Point out every Plasmodium parasite.
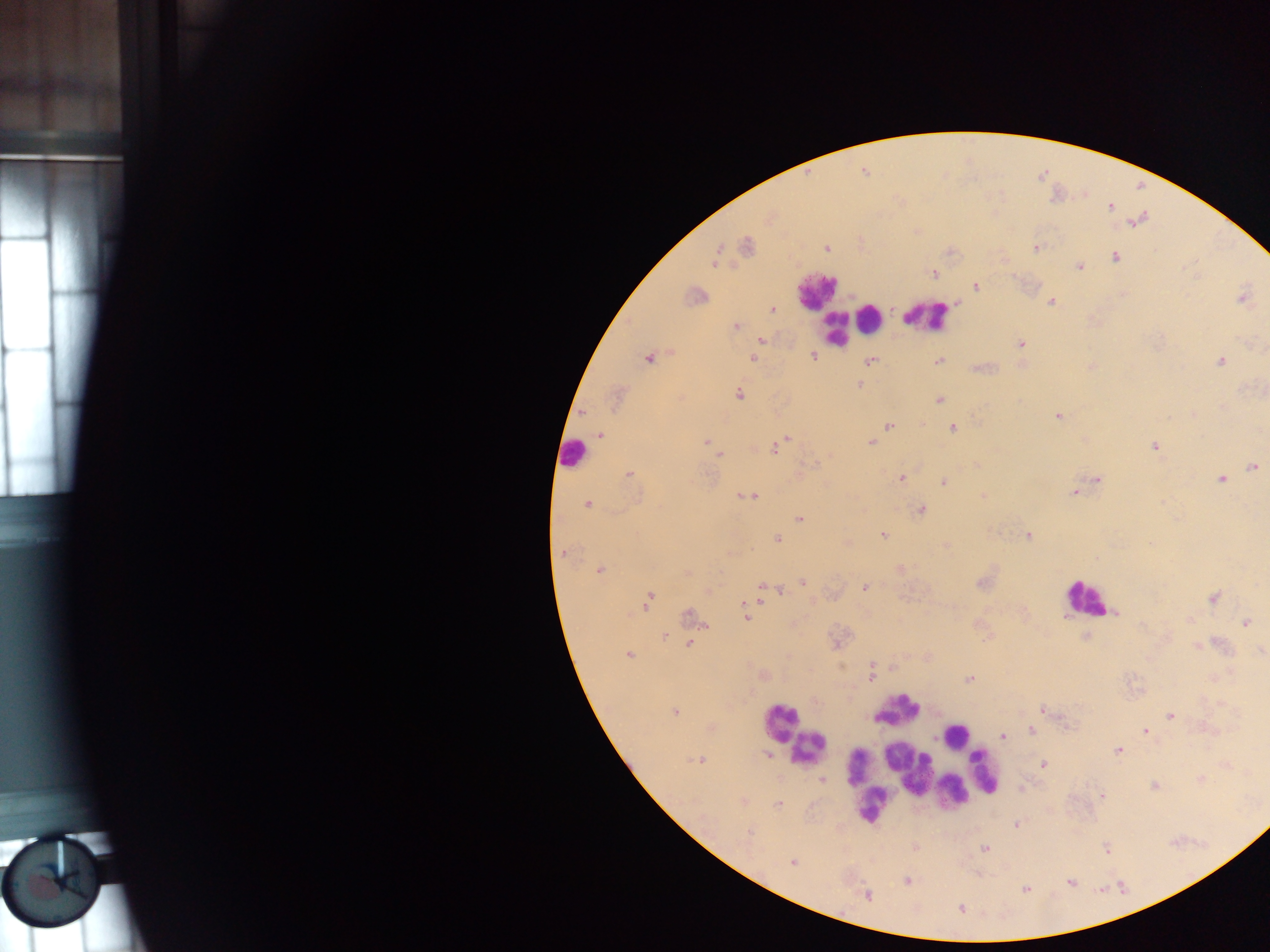

Approximate centers as x y in pixels.
Plasmodium parasites: 1110 206; 1136 222; 746 246; 827 248; 1036 248; 1115 257; 714 259; 1079 266; 933 273; 976 286; 694 297; 1242 298; 1051 302; 772 309; 735 326; 761 340; 1021 344; 814 357; 648 358; 753 358; 871 361; 938 361; 1220 362; 859 385; 739 394; 615 398; 940 399; 1193 414; 1058 415; 889 425; 953 429; 601 434; 786 440; 706 442; 870 443; 1155 446; 775 447; 712 448; 718 453; 1253 467; 630 474; 901 478; 1221 479; 1097 480; 944 482; 1074 492; 747 496; 983 496; 587 505; 921 509; 800 518; 882 534; 1028 535; 777 540; 564 553; 901 569; 599 570; 687 572; 802 582; 865 587; 769 589; 778 590; 1213 598; 649 600; 691 617; 747 618; 1245 622; 664 637; 690 644; 1197 646; 628 654; 872 670; 871 676; 969 680; 1043 711; 675 713; 1171 716; 1033 731; 1145 731; 1002 736; 1118 751; 768 755; 699 760; 1044 764; 1200 779; 822 780; 1154 786; 1101 795; 778 805; 1017 825; 748 832; 1107 848; 984 849; 792 862; 907 881; 1070 882; 1026 889; 867 895; 961 909.

Leukocyte locations: 817 290; 926 315; 870 317; 835 331; 572 454; 1084 597; 899 710; 779 721; 956 735; 808 748; 858 767; 907 768; 985 772; 966 782; 866 787; 952 791; 871 806. Photographed through a microscope with a mobile-phone camera. Image is 1270×952 pixels. Thick blood smear. Single field of view. Sample from Ghana.